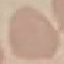
Summary:
  - Result: no malaria parasites detected
  - Preparation: thin blood smear
  - Capture: smartphone camera at the microscope eyepiece
  - Image type: cell patch, automatically extracted from a larger field of view and resized to 64 × 64 pixels
  - Stain: Giemsa